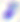
Micrograph. 400x magnification. Toxoplasma gondii is seen.